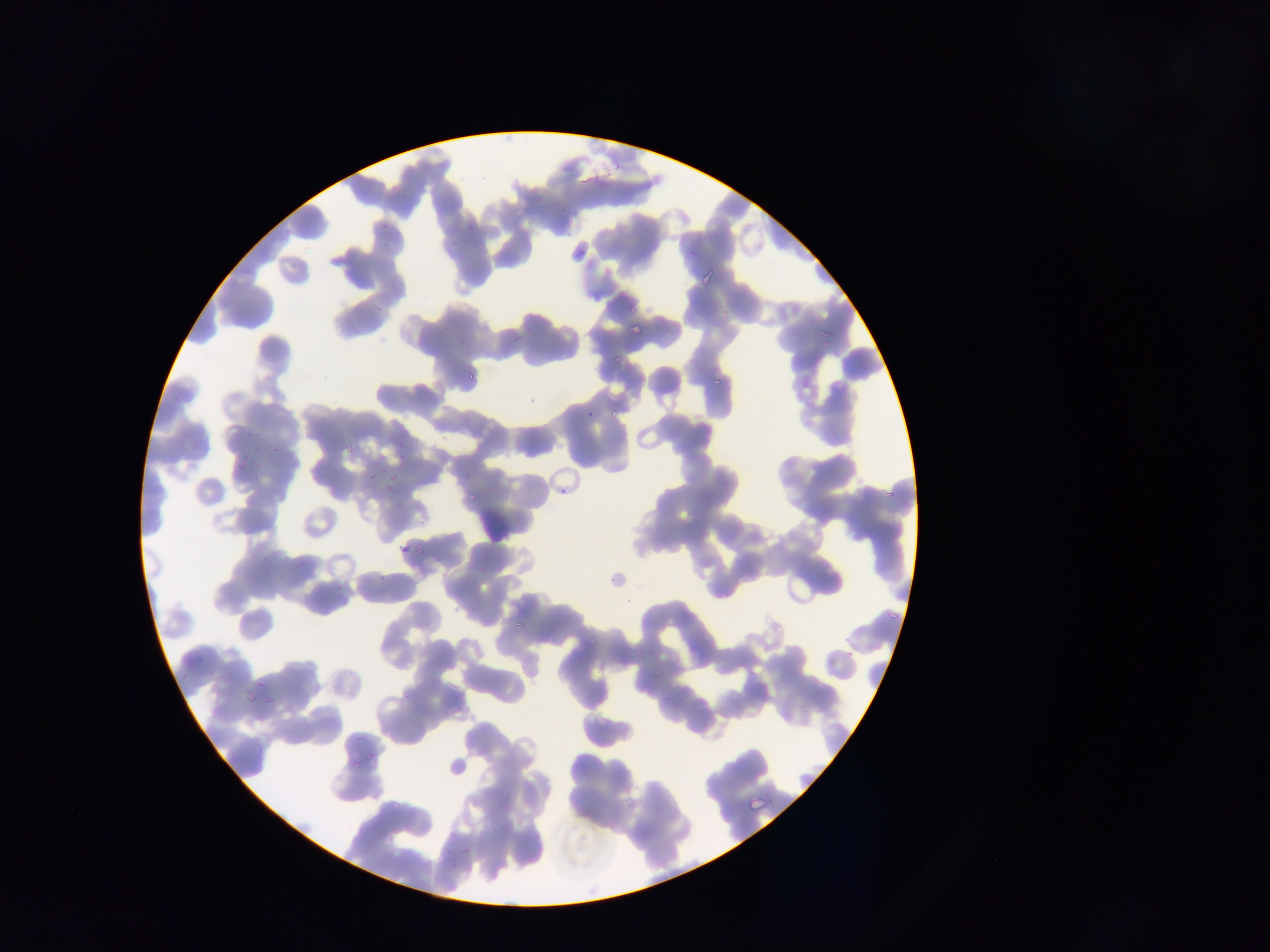 Approximate bounding boxes as (left, top, right, bottom) in pixels. Plasmodium parasite locations: (528, 198, 546, 210), (375, 219, 386, 232), (459, 219, 480, 233), (445, 240, 453, 250), (684, 245, 703, 257), (571, 249, 588, 261), (695, 262, 721, 287), (625, 304, 636, 314), (628, 318, 651, 335), (442, 322, 450, 337), (819, 325, 834, 345), (456, 328, 473, 347), (509, 331, 527, 348), (611, 346, 630, 363), (466, 369, 477, 386), (710, 377, 726, 385), (584, 407, 596, 420), (608, 407, 619, 418), (269, 434, 283, 453), (347, 439, 366, 451), (392, 445, 412, 462), (231, 446, 254, 475), (244, 456, 270, 473), (363, 470, 377, 481), (556, 476, 579, 497), (882, 476, 899, 501), (379, 478, 398, 493), (466, 485, 477, 502), (397, 540, 416, 554), (413, 541, 427, 556), (372, 577, 394, 600), (414, 603, 448, 629), (511, 608, 531, 630), (884, 608, 902, 622), (846, 640, 858, 659), (631, 645, 646, 656), (193, 650, 205, 664), (252, 674, 265, 688), (239, 690, 255, 703), (263, 691, 280, 708), (658, 695, 670, 701), (794, 695, 815, 713), (348, 729, 365, 742), (361, 748, 380, 764), (446, 754, 468, 776), (351, 758, 363, 775), (746, 787, 772, 810), (458, 845, 476, 858), (444, 850, 454, 866). Photographed through a microscope with a mobile-phone camera. Image is 1270×952 pixels. Sample from Ghana. One field of view. Thin blood smear.